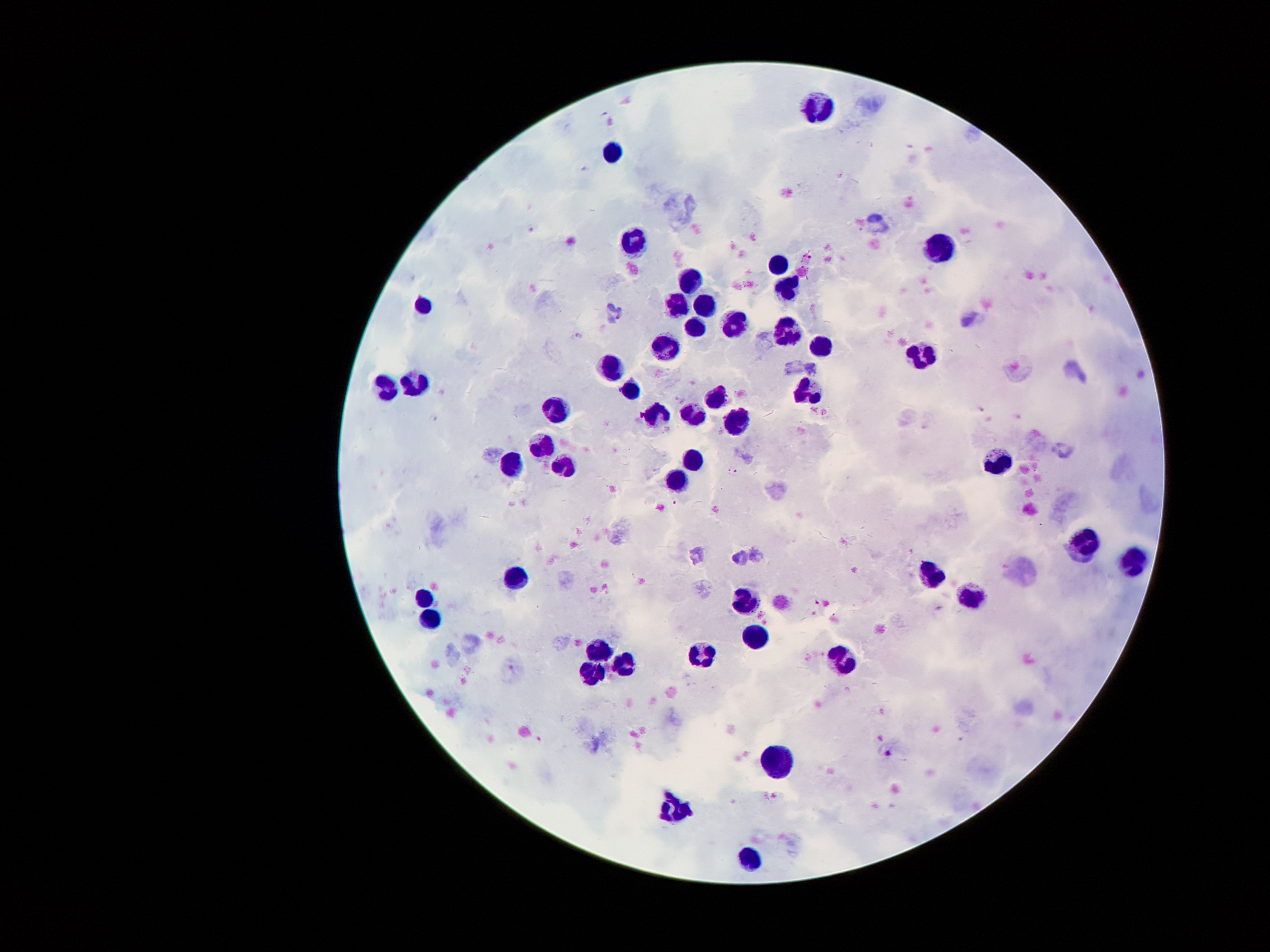
Approximate centers as (x, y) in pixels.
Summary:
  - Malaria parasite locations: (580, 336), (982, 409), (727, 472), (736, 473), (674, 503), (816, 604), (887, 753)
  - Leukocyte locations: (820, 105), (610, 151), (633, 243), (938, 248), (782, 266), (686, 277), (790, 290), (422, 305), (675, 307), (708, 307), (733, 324), (694, 326), (786, 330), (667, 347), (821, 347), (923, 355), (613, 368), (417, 381), (628, 386), (389, 389), (807, 394), (718, 399), (560, 411), (694, 413), (658, 415), (737, 418), (545, 447), (1000, 458), (691, 459), (511, 466), (563, 467), (677, 479), (1085, 541), (1132, 563), (929, 572), (514, 577), (744, 597), (970, 597), (423, 598), (430, 616), (756, 634), (596, 651), (700, 657), (843, 661), (624, 662), (589, 672), (779, 761), (677, 811), (748, 858)
  - Stain: Giemsa
  - Capture: smartphone camera through the microscope eyepiece
  - Preparation: thick blood smear
  - Magnification: 100x
  - Image size: 1270×952 pixels
  - Patient malaria status: infected with Plasmodium falciparum
  - Field of view: one from this slide